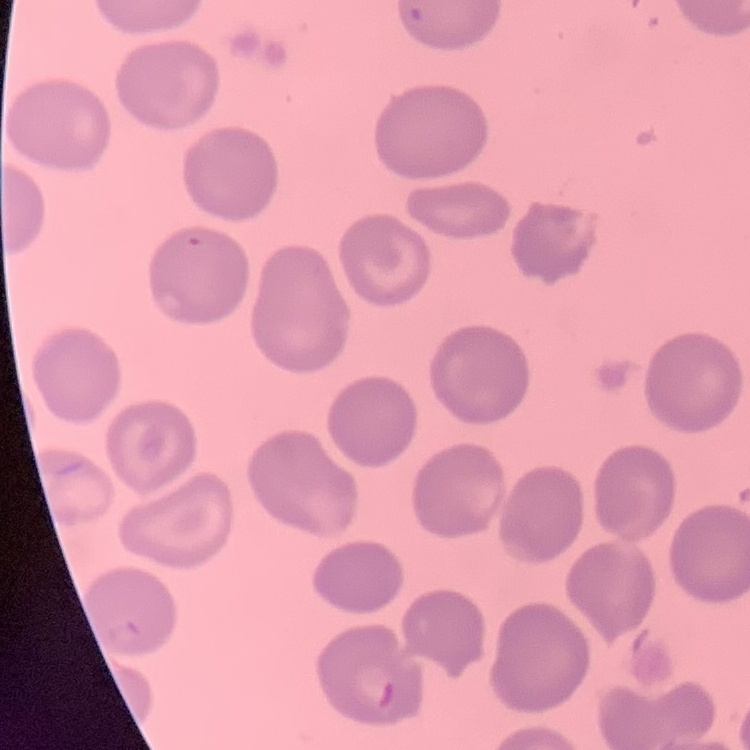
Summary:
  - Red blood cell morphology: no rouleaux formation
  - Stain: Field's or Giemsa
  - Preparation: thin blood film
  - Image type: square crop of a larger photomicrograph